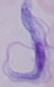

identification = trypanosome
modality = photomicrograph
magnification = 1000x